Name the parasite shown.
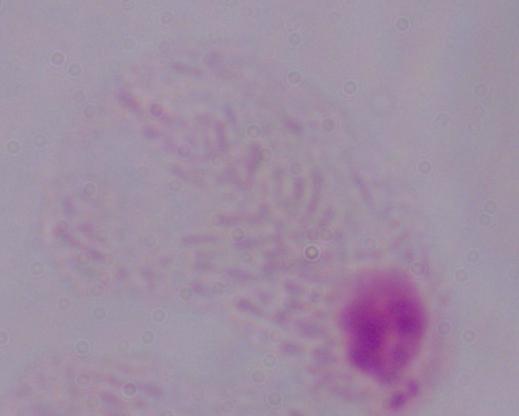

A trichomonad.

magnification: 1000x
modality: photomicrograph